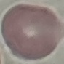

{
  "malaria_status": "uninfected",
  "image_type": "cell patch, automatically extracted from a larger field of view and resized to 64 × 64 pixels",
  "preparation": "thin blood film",
  "capture": "smartphone through the microscope eyepiece",
  "stain": "Giemsa"
}